Identify the cell.
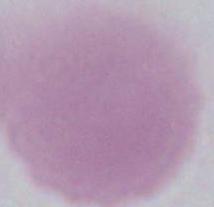
This is an erythrocyte.

Summary:
  - Magnification: 1000x
  - Modality: photomicrograph